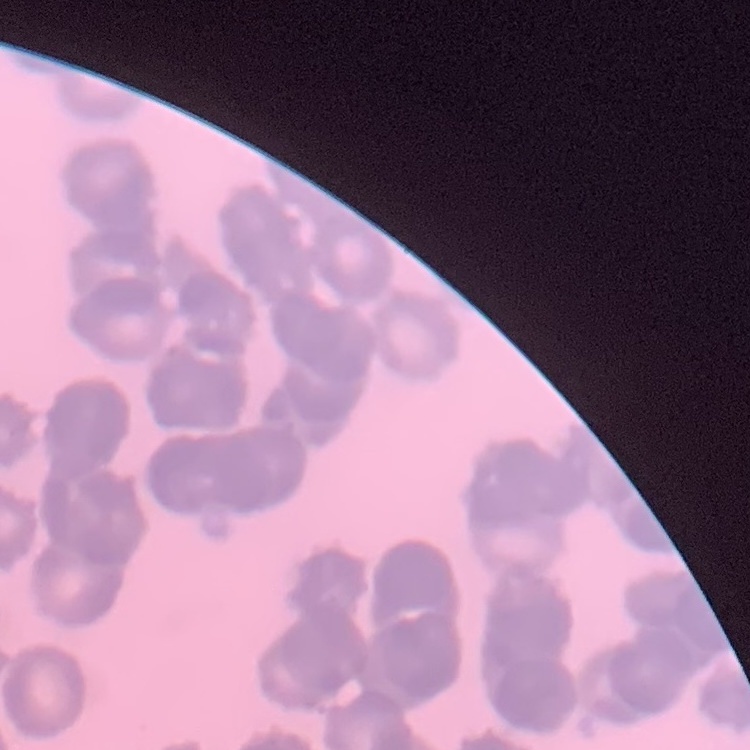

Summary:
  - Red blood cell morphology: rouleaux formation
  - Preparation: thin blood film
  - Image type: square crop of a larger photomicrograph
  - Stain: Field's or Giemsa